Classify this cell by malaria status.
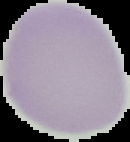

It is uninfected.

Image is 130×142 pixels. From a thin blood film. Cell region segmented out of the field of view; the surrounding area is masked to black.